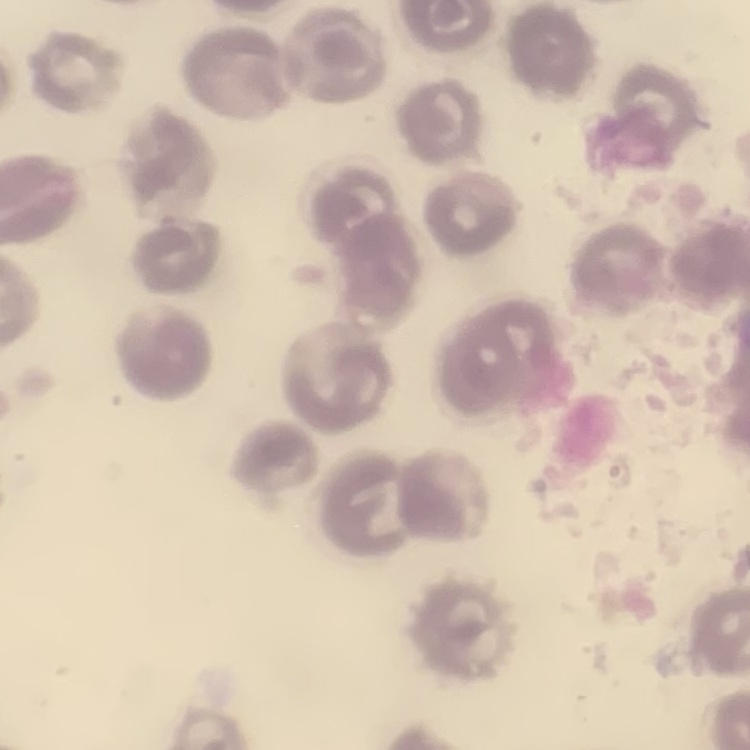
Summary:
  - Red blood cell morphology: no rouleaux formation
  - Image type: square crop of a larger photomicrograph
  - Preparation: thin blood film
  - Stain: Field's or Giemsa